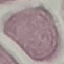

Summary:
  - Result: negative for malaria parasites
  - Preparation: thin blood smear
  - Stain: Giemsa
  - Image type: automatically extracted cell patch, resized to 64 × 64 pixels
  - Capture: smartphone through the microscope eyepiece